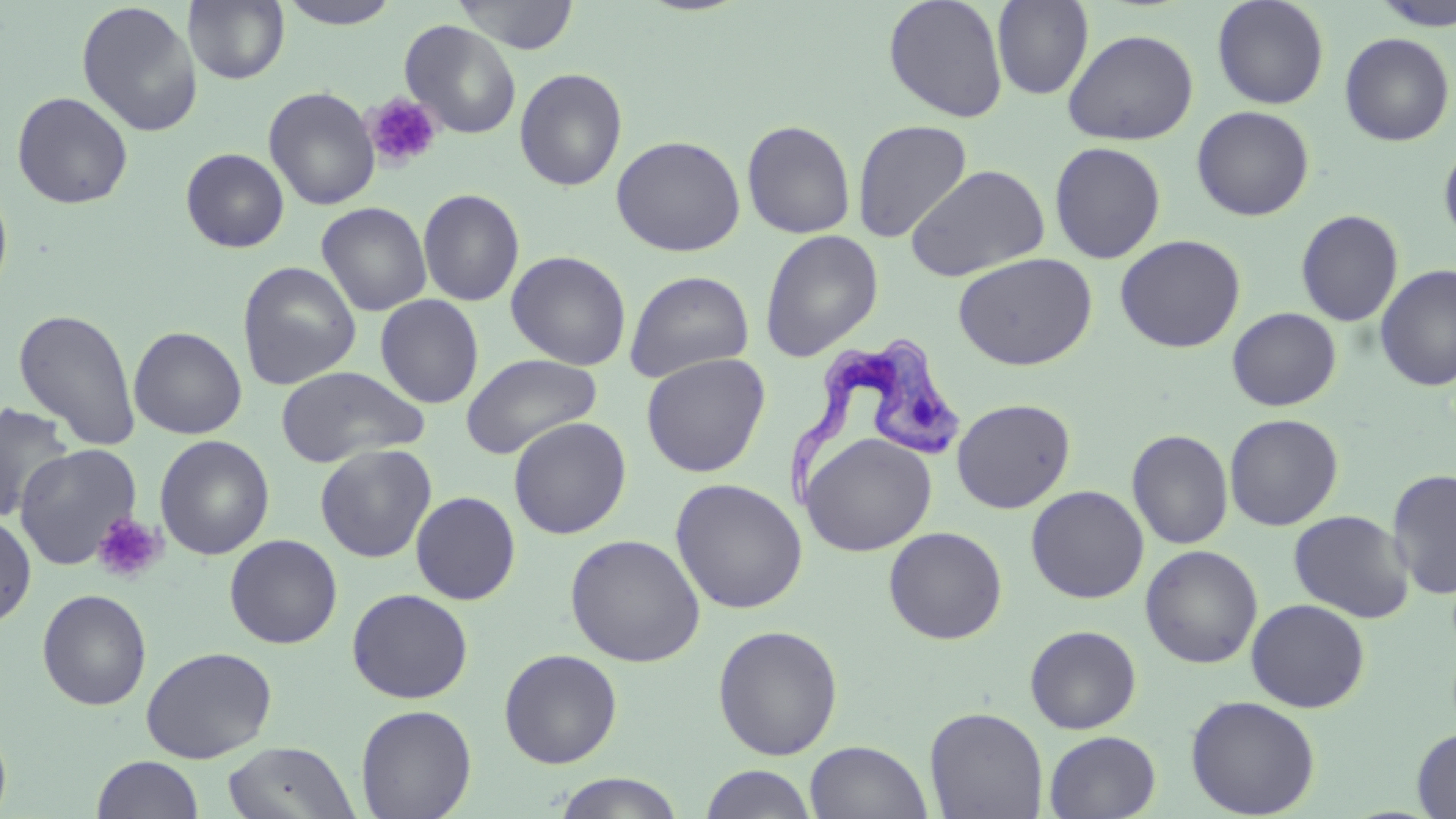 Approximate bounding boxes as named x1/y1/x2/y2 corners in pixels. Platelet locations: (x1=363, y1=92, x2=443, y2=171), (x1=91, y1=512, x2=167, y2=584). Uninfected red blood cell locations: (x1=183, y1=0, x2=290, y2=85), (x1=453, y1=0, x2=579, y2=54), (x1=883, y1=0, x2=1009, y2=123), (x1=992, y1=0, x2=1093, y2=99), (x1=1211, y1=0, x2=1330, y2=109), (x1=76, y1=1, x2=202, y2=137), (x1=277, y1=1, x2=402, y2=29), (x1=1372, y1=1, x2=1456, y2=31), (x1=400, y1=20, x2=522, y2=139), (x1=1062, y1=28, x2=1199, y2=145), (x1=1339, y1=32, x2=1454, y2=146), (x1=514, y1=68, x2=628, y2=191), (x1=263, y1=86, x2=380, y2=211), (x1=11, y1=91, x2=134, y2=210), (x1=1191, y1=105, x2=1314, y2=221), (x1=851, y1=118, x2=973, y2=243), (x1=741, y1=119, x2=856, y2=239), (x1=610, y1=135, x2=746, y2=256), (x1=1438, y1=138, x2=1456, y2=248), (x1=1049, y1=141, x2=1166, y2=264), (x1=180, y1=148, x2=289, y2=253), (x1=906, y1=164, x2=1050, y2=282), (x1=0, y1=179, x2=13, y2=304), (x1=418, y1=188, x2=525, y2=307), (x1=316, y1=202, x2=432, y2=316), (x1=1295, y1=209, x2=1404, y2=327), (x1=759, y1=229, x2=884, y2=361), (x1=1114, y1=234, x2=1246, y2=353), (x1=506, y1=250, x2=632, y2=370), (x1=952, y1=252, x2=1097, y2=370), (x1=237, y1=260, x2=361, y2=390), (x1=1375, y1=262, x2=1456, y2=392), (x1=624, y1=270, x2=754, y2=383), (x1=375, y1=294, x2=484, y2=409), (x1=13, y1=307, x2=142, y2=452), (x1=1227, y1=307, x2=1342, y2=412), (x1=129, y1=326, x2=247, y2=439), (x1=640, y1=352, x2=771, y2=477), (x1=460, y1=353, x2=602, y2=459), (x1=275, y1=365, x2=429, y2=468), (x1=952, y1=398, x2=1076, y2=513), (x1=0, y1=402, x2=74, y2=522), (x1=1224, y1=413, x2=1344, y2=531), (x1=507, y1=417, x2=632, y2=540), (x1=1127, y1=429, x2=1233, y2=550), (x1=801, y1=432, x2=936, y2=556), (x1=154, y1=435, x2=275, y2=560), (x1=14, y1=443, x2=142, y2=570), (x1=316, y1=444, x2=437, y2=562), (x1=1387, y1=469, x2=1456, y2=600), (x1=670, y1=478, x2=808, y2=614), (x1=1026, y1=485, x2=1149, y2=603), (x1=410, y1=491, x2=521, y2=605), (x1=1288, y1=509, x2=1415, y2=623), (x1=0, y1=512, x2=37, y2=629), (x1=883, y1=526, x2=1007, y2=644), (x1=565, y1=533, x2=706, y2=667), (x1=224, y1=534, x2=343, y2=649), (x1=1140, y1=544, x2=1263, y2=669), (x1=346, y1=588, x2=473, y2=704), (x1=37, y1=589, x2=152, y2=711), (x1=1246, y1=598, x2=1370, y2=713), (x1=712, y1=624, x2=844, y2=760), (x1=1024, y1=624, x2=1142, y2=734), (x1=141, y1=645, x2=278, y2=763), (x1=499, y1=648, x2=622, y2=768), (x1=1185, y1=695, x2=1321, y2=818), (x1=355, y1=704, x2=477, y2=819), (x1=924, y1=706, x2=1049, y2=819), (x1=0, y1=719, x2=12, y2=819), (x1=1412, y1=727, x2=1456, y2=818), (x1=1043, y1=731, x2=1161, y2=818), (x1=804, y1=740, x2=933, y2=819), (x1=223, y1=741, x2=360, y2=819), (x1=91, y1=755, x2=205, y2=818), (x1=699, y1=764, x2=818, y2=819), (x1=553, y1=772, x2=685, y2=819). Trypanosoma brucei locations: (x1=781, y1=342, x2=963, y2=514). Slide-level diagnosis: Trypanosoma brucei. Thin blood smear. 1000x magnification. Single field of view. Image is 1456×819 pixels. May-Grünwald-Giemsa-stained preparation. Light microscopy.